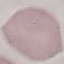

Result: no malaria parasites detected. Thin blood smear. Giemsa stain. Photographed with a smartphone camera at the microscope eyepiece. Automatically extracted cell patch, resized to 64 × 64 pixels.